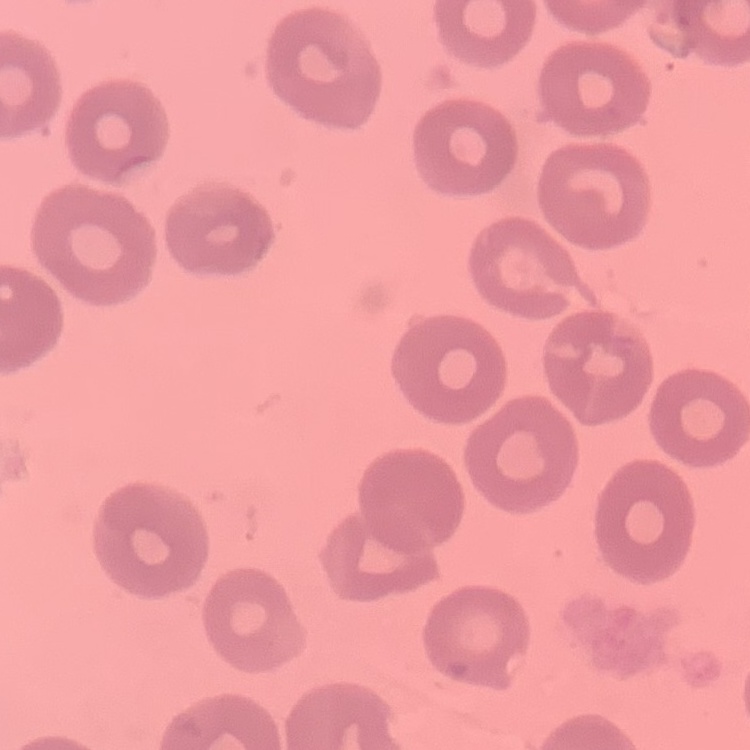
Summary:
  - Red blood cell morphology: no rouleaux formation
  - Image type: one tile cut from a larger photomicrograph
  - Preparation: thin blood film
  - Stain: Field's or Giemsa